Identify the parasite.
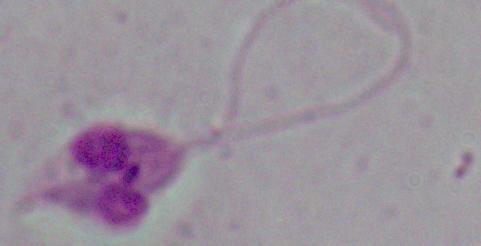
Leishmania.

Summary:
  - Magnification: 1000x
  - Modality: micrograph